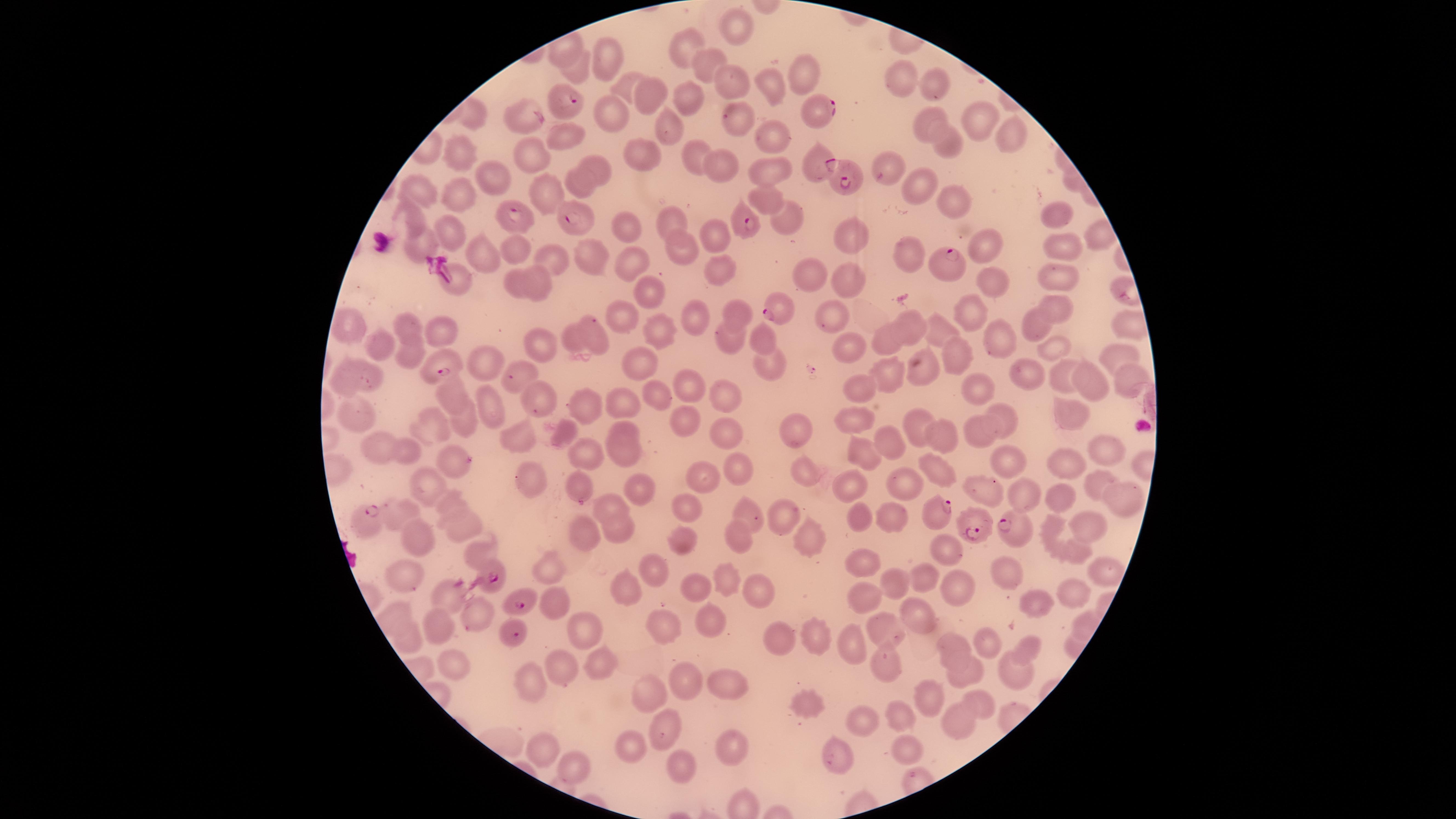
Approximate marker points as (x, y) in pixels. Uninfected RBCs: (736, 27), (683, 48), (605, 51), (703, 61), (579, 68), (807, 74), (896, 77), (728, 81), (931, 84), (623, 85), (776, 87), (649, 94), (688, 96), (528, 114), (478, 117), (610, 118), (979, 120), (925, 124), (670, 125), (738, 125), (567, 134), (1012, 134), (771, 136), (948, 143), (460, 149), (696, 153), (534, 156), (646, 156), (596, 162), (888, 164), (717, 167), (773, 172), (495, 175), (579, 183), (917, 184), (419, 190), (549, 191), (457, 195), (766, 199), (960, 203), (413, 215), (1059, 215), (787, 222), (672, 223), (628, 227), (454, 231), (714, 234), (854, 240), (423, 244), (986, 245), (1057, 246), (682, 248), (515, 249), (480, 254), (908, 255), (592, 257), (556, 259), (631, 262), (717, 271), (809, 275), (457, 278), (1057, 278), (995, 279), (846, 281), (541, 282), (517, 283), (645, 294), (1055, 307), (737, 312), (967, 315), (619, 317), (696, 317), (835, 318), (911, 321), (346, 325), (409, 327), (1033, 328), (444, 329), (655, 329), (935, 330), (593, 338), (764, 338), (995, 338), (576, 339), (732, 340), (886, 341), (1057, 344), (543, 345), (381, 347), (851, 349), (1115, 352), (412, 356), (957, 356), (487, 361), (640, 365), (771, 370), (925, 370), (1061, 370), (1026, 373), (344, 374), (886, 375), (371, 376), (523, 377), (1140, 380), (1094, 386), (858, 387), (687, 389), (976, 389), (456, 391), (722, 392), (657, 396), (545, 397), (489, 400), (621, 400), (587, 405), (1002, 409), (1067, 412), (356, 415), (465, 418), (851, 420), (690, 422), (920, 422), (436, 425), (624, 428), (796, 430), (975, 430), (567, 432), (730, 434), (515, 437), (940, 437), (891, 445), (1105, 447), (382, 448), (586, 451), (408, 452), (620, 452), (860, 454), (1009, 459), (457, 461), (1062, 466), (735, 468), (701, 472), (939, 472), (804, 473), (529, 474), (1097, 480), (585, 481), (905, 483), (431, 485), (851, 487), (978, 489), (641, 490), (1025, 494), (1064, 496), (1123, 500), (605, 502), (454, 505), (692, 509), (403, 511), (748, 515), (784, 517), (862, 517), (892, 517), (467, 523), (1094, 523), (620, 528), (1051, 532), (586, 534), (419, 535), (739, 536), (682, 539), (811, 539), (946, 549), (480, 550), (1079, 556), (865, 564), (548, 568), (655, 569), (1008, 570), (405, 572), (924, 574), (1104, 575), (722, 578), (893, 583), (958, 584), (1075, 590), (697, 591), (755, 591), (625, 594), (863, 596), (448, 597), (558, 602), (1042, 605), (395, 612), (920, 614), (476, 618), (434, 623), (716, 624), (665, 625), (583, 627), (884, 631), (815, 632), (786, 638), (987, 640), (414, 643), (849, 643), (952, 644), (1029, 646), (602, 661), (460, 666), (888, 666), (568, 667), (1016, 671), (965, 675), (726, 682), (684, 683), (530, 684), (647, 695), (927, 696), (979, 704), (806, 707), (903, 717), (956, 720), (864, 721), (672, 726), (630, 746), (540, 749), (733, 749), (907, 749), (834, 757), (682, 765), (569, 770). Parasitized RBCs: (560, 104), (817, 110), (814, 165), (854, 177), (576, 217), (518, 218), (748, 225), (951, 262), (782, 308), (445, 364), (936, 514), (365, 520), (976, 528), (1011, 528), (490, 570), (520, 596), (506, 631). Giemsa-stained preparation. The visible region is circular. Photographed with a smartphone camera through the microscope eyepiece. Thin blood smear. Image is 1456×819 pixels. Presence: malaria parasites identified. Species: Plasmodium falciparum. One field of view of the specimen.